Assess this cell for malaria.
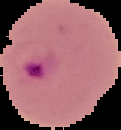

It is parasitized.

From a thin blood film. Image is 121×130 pixels. The area outside the segmented cell region is set to black.